Classify this cell by malaria status.
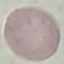
Uninfected.

Thin blood smear. Giemsa stain. Automatically extracted cell patch, resized to 64 × 64 pixels. Acquired by smartphone through the microscope eyepiece.